Name the parasite shown.
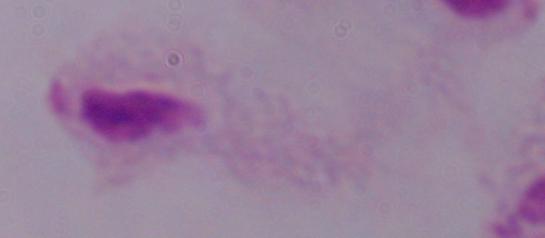
This is a trichomonad.

modality = photomicrograph
magnification = 1000x